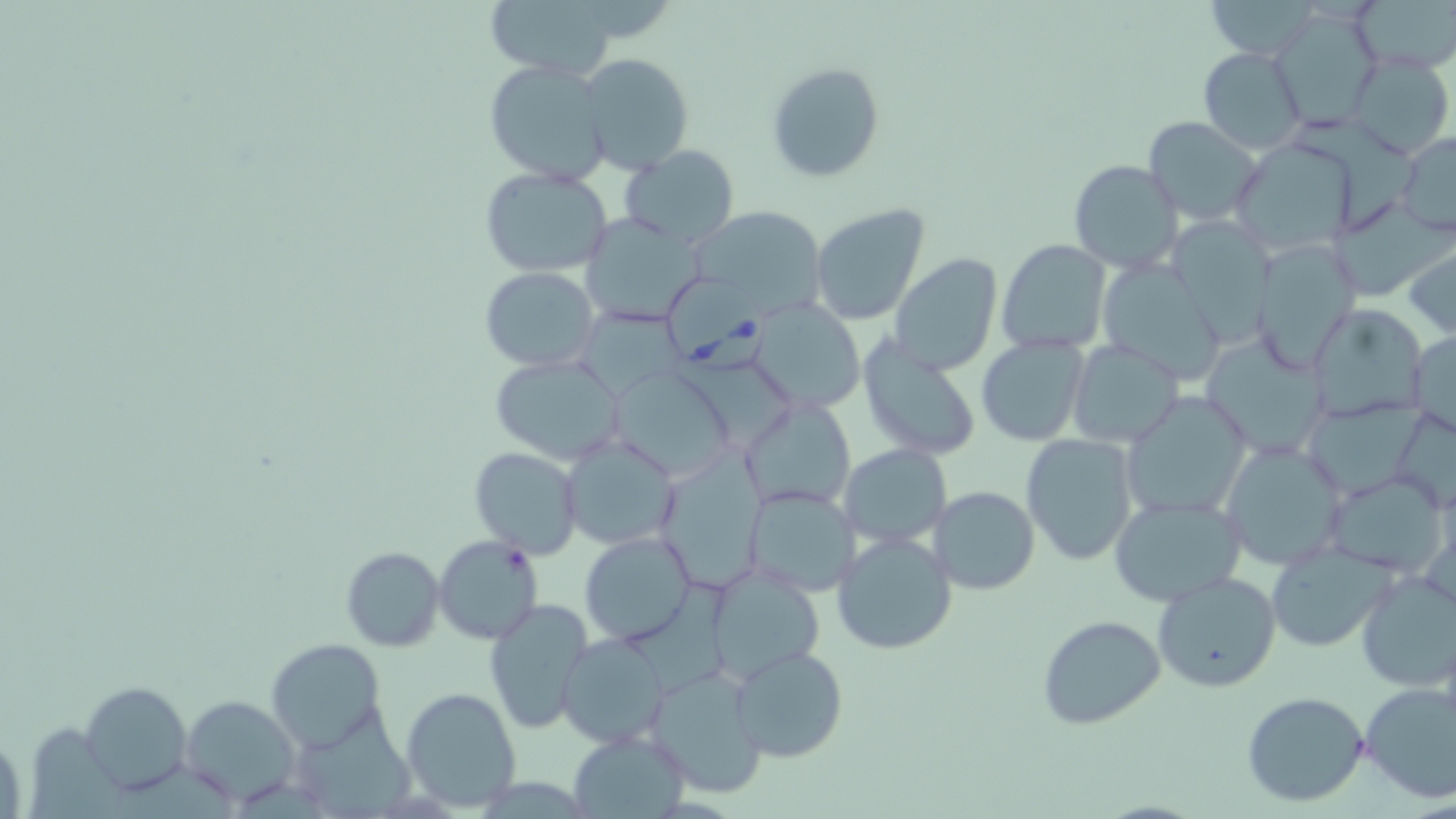

{
  "slide_level_diagnosis": "Babesia divergens",
  "field_of_view": "one of a larger specimen",
  "stain": "May-Grünwald-Giemsa",
  "modality": "optical microscopy",
  "uninfected_red_blood_cell_locations": "approximate bounding boxes as (x1, y1, x2, y2) in pixels: (488, 0, 621, 80), (1351, 0, 1456, 76), (1272, 6, 1383, 131), (1197, 46, 1307, 155), (1344, 51, 1455, 160), (576, 53, 695, 175), (483, 59, 614, 187), (766, 61, 886, 184), (1142, 116, 1264, 227), (1395, 131, 1456, 236), (1231, 140, 1357, 255), (619, 145, 738, 248), (1067, 159, 1184, 274), (479, 166, 616, 277), (1329, 196, 1451, 300), (689, 203, 826, 312), (809, 203, 930, 327), (580, 214, 705, 327), (1169, 218, 1276, 339), (995, 238, 1112, 355), (1404, 238, 1456, 340), (1248, 239, 1361, 373), (888, 252, 1004, 374), (1098, 256, 1230, 383), (480, 267, 599, 371), (752, 299, 863, 413), (1308, 304, 1431, 423), (570, 305, 692, 399), (1408, 327, 1455, 435), (856, 333, 983, 461), (1201, 334, 1333, 461), (975, 335, 1089, 446), (1068, 340, 1184, 449), (489, 354, 628, 464), (609, 364, 733, 481), (1122, 390, 1253, 521), (743, 397, 856, 512), (1301, 399, 1425, 502), (1022, 434, 1139, 564), (562, 436, 679, 550), (1218, 439, 1349, 571), (664, 441, 765, 603), (840, 444, 951, 547), (469, 447, 582, 559), (1323, 470, 1450, 580), (743, 486, 860, 594), (932, 486, 1039, 595), (1106, 494, 1247, 606), (831, 530, 958, 655), (579, 531, 696, 646), (433, 534, 541, 644), (1265, 544, 1392, 652), (340, 546, 445, 651), (711, 567, 824, 680), (1353, 568, 1456, 693), (1152, 571, 1282, 693), (482, 599, 596, 737), (1036, 614, 1166, 730), (556, 634, 669, 747), (267, 637, 384, 748), (731, 644, 848, 764), (644, 665, 765, 798), (80, 682, 191, 795), (1360, 683, 1455, 804), (401, 686, 521, 810), (1240, 691, 1370, 808), (181, 694, 300, 807), (298, 711, 422, 819), (568, 730, 691, 818)",
  "magnification": "1000x",
  "babesia_divergens_infected_red_blood_cell_locations": "approximate bounding boxes as (x1, y1, x2, y2) in pixels: (670, 275, 766, 378)",
  "image_size": "1456×819 pixels",
  "preparation": "thin blood smear"
}